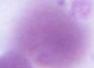
Micrograph. 1000x magnification. A red blood cell is shown.